Outline each Plasmodium ovale-infected red blood cell.
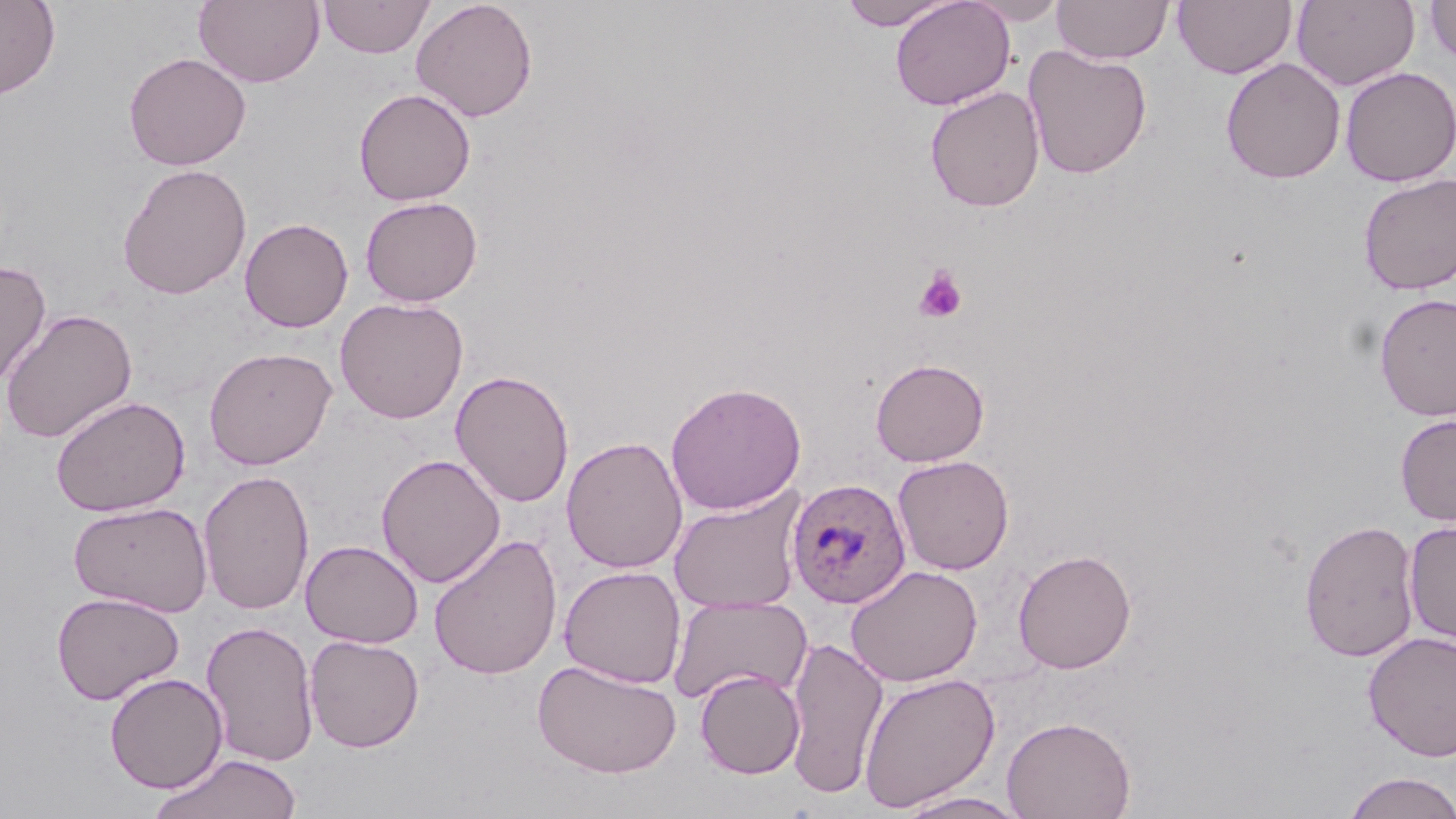
Approximate bounding boxes as named x1/y1/x2/y2 corners in pixels.
Plasmodium ovale-infected red blood cells: (x1=786, y1=477, x2=912, y2=609).

Summary:
  - Uninfected red blood cell locations: (x1=0, y1=0, x2=61, y2=99), (x1=193, y1=0, x2=324, y2=88), (x1=319, y1=0, x2=435, y2=59), (x1=410, y1=0, x2=538, y2=122), (x1=839, y1=0, x2=955, y2=30), (x1=890, y1=0, x2=1015, y2=110), (x1=965, y1=0, x2=1069, y2=25), (x1=1052, y1=0, x2=1173, y2=64), (x1=1172, y1=0, x2=1296, y2=80), (x1=1292, y1=0, x2=1419, y2=91), (x1=1424, y1=0, x2=1456, y2=66), (x1=1022, y1=44, x2=1153, y2=180), (x1=123, y1=52, x2=251, y2=171), (x1=1220, y1=57, x2=1346, y2=184), (x1=1339, y1=66, x2=1455, y2=187), (x1=925, y1=86, x2=1046, y2=213), (x1=353, y1=87, x2=476, y2=206), (x1=116, y1=163, x2=252, y2=299), (x1=1357, y1=172, x2=1456, y2=295), (x1=359, y1=196, x2=483, y2=307), (x1=239, y1=217, x2=353, y2=332), (x1=0, y1=259, x2=52, y2=389), (x1=1373, y1=292, x2=1456, y2=421), (x1=334, y1=296, x2=469, y2=424), (x1=1, y1=308, x2=138, y2=444), (x1=203, y1=346, x2=337, y2=470), (x1=870, y1=358, x2=990, y2=467), (x1=450, y1=369, x2=575, y2=508), (x1=665, y1=381, x2=806, y2=515), (x1=50, y1=395, x2=190, y2=518), (x1=1395, y1=413, x2=1456, y2=527), (x1=561, y1=435, x2=688, y2=574), (x1=376, y1=453, x2=506, y2=588), (x1=892, y1=455, x2=1014, y2=575), (x1=198, y1=468, x2=315, y2=616), (x1=668, y1=487, x2=807, y2=614), (x1=68, y1=500, x2=213, y2=616), (x1=1300, y1=519, x2=1420, y2=661), (x1=1402, y1=519, x2=1456, y2=645), (x1=428, y1=533, x2=563, y2=680), (x1=301, y1=539, x2=423, y2=648), (x1=1012, y1=549, x2=1137, y2=674), (x1=846, y1=564, x2=983, y2=687), (x1=558, y1=565, x2=687, y2=688), (x1=51, y1=591, x2=185, y2=705), (x1=668, y1=593, x2=812, y2=705), (x1=200, y1=620, x2=319, y2=767), (x1=1363, y1=631, x2=1456, y2=761), (x1=304, y1=635, x2=425, y2=752), (x1=784, y1=635, x2=889, y2=799), (x1=531, y1=658, x2=683, y2=778), (x1=695, y1=669, x2=805, y2=779), (x1=104, y1=672, x2=227, y2=793), (x1=857, y1=672, x2=1000, y2=811), (x1=1002, y1=715, x2=1136, y2=819), (x1=148, y1=753, x2=303, y2=819), (x1=1339, y1=771, x2=1456, y2=819), (x1=894, y1=791, x2=1031, y2=819)
  - Platelet locations: (x1=915, y1=267, x2=968, y2=323)
  - Slide-level diagnosis: Plasmodium ovale
  - Magnification: 1000x
  - Image size: 1456×819 pixels
  - Field of view: one of a larger specimen
  - Preparation: thin blood film
  - Modality: optical microscopy
  - Stain: May-Grünwald-Giemsa